Locate every Plasmodium parasite.
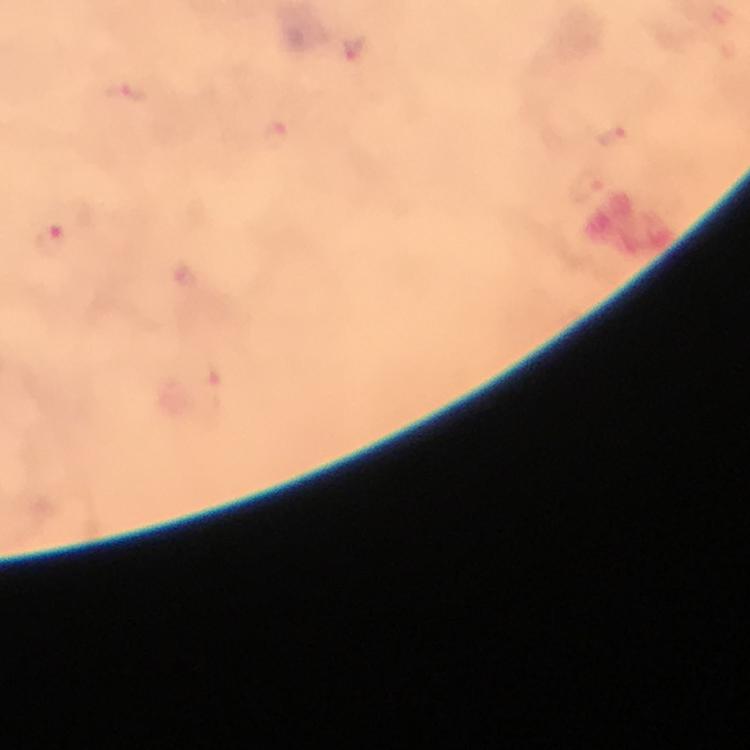

Approximate centers as {x, y} in pixels.
Plasmodium parasites: {127, 94}, {275, 135}, {612, 136}, {586, 187}, {53, 242}.

Giemsa stain. From a diagnostic examination for malaria. A crop from one field of view. Image is 750×750 pixels. At 100x magnification. Photographed with a smartphone mounted on the microscope. Thick smear. Immersion oil applied.